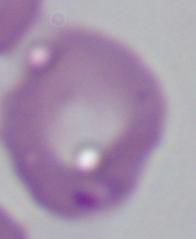

{
  "identification": "Babesia",
  "magnification": "1000x",
  "modality": "photomicrograph"
}